Locate every Plasmodium parasite.
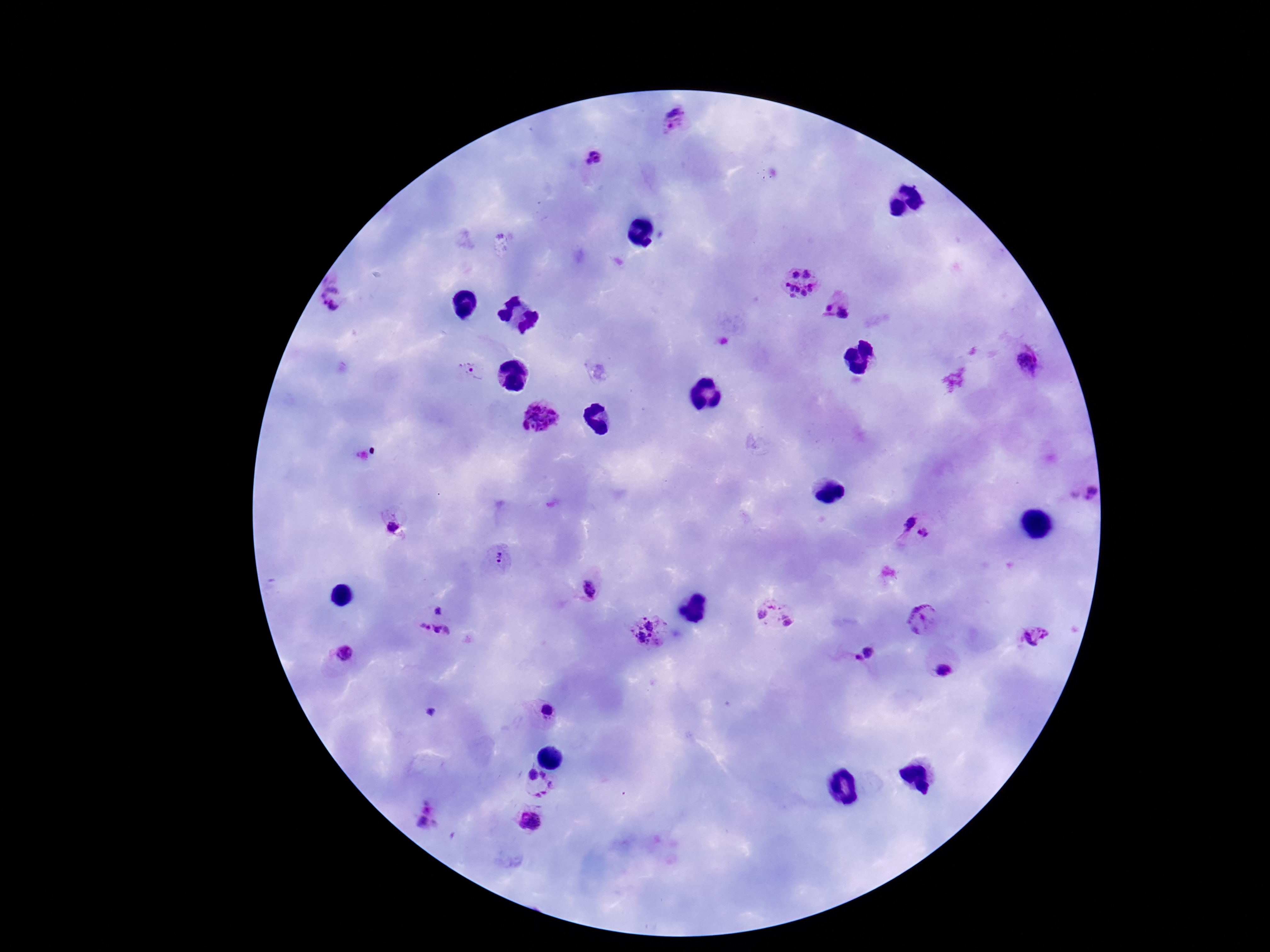

Approximate centers as (x, y) in pixels.
Plasmodium parasites: (673, 123), (596, 159), (797, 283), (335, 296), (837, 304), (1026, 360), (471, 370), (541, 416), (1088, 487), (902, 519), (392, 523), (926, 534), (501, 558), (588, 587), (764, 607), (437, 609), (789, 616), (925, 618), (651, 629), (1035, 635), (433, 638), (344, 653), (868, 653), (859, 660), (941, 668), (546, 709), (430, 712), (532, 772), (558, 785), (426, 817), (529, 822).

{
  "stain": "Giemsa",
  "patient_malaria_status": "positive",
  "magnification": "100x",
  "field_of_view": "single",
  "capture": "smartphone camera through the microscope eyepiece",
  "image_size": "1270×952 pixels",
  "preparation": "thick blood smear"
}